State which cell type is depicted.
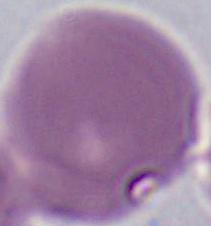
This is an erythrocyte.

1000x magnification. Micrograph.